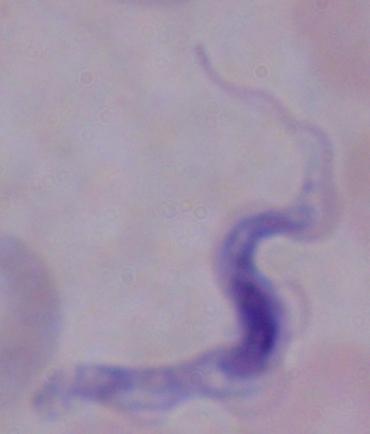
Summary:
  - Identification: trypanosome
  - Modality: micrograph
  - Magnification: 1000x